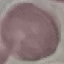

Summary:
  - Result: negative for malaria parasites
  - Image type: automatically extracted cell patch, resized to 64 × 64 pixels
  - Stain: Giemsa
  - Capture: smartphone camera at the microscope eyepiece
  - Preparation: thin blood film